State the preparation type.
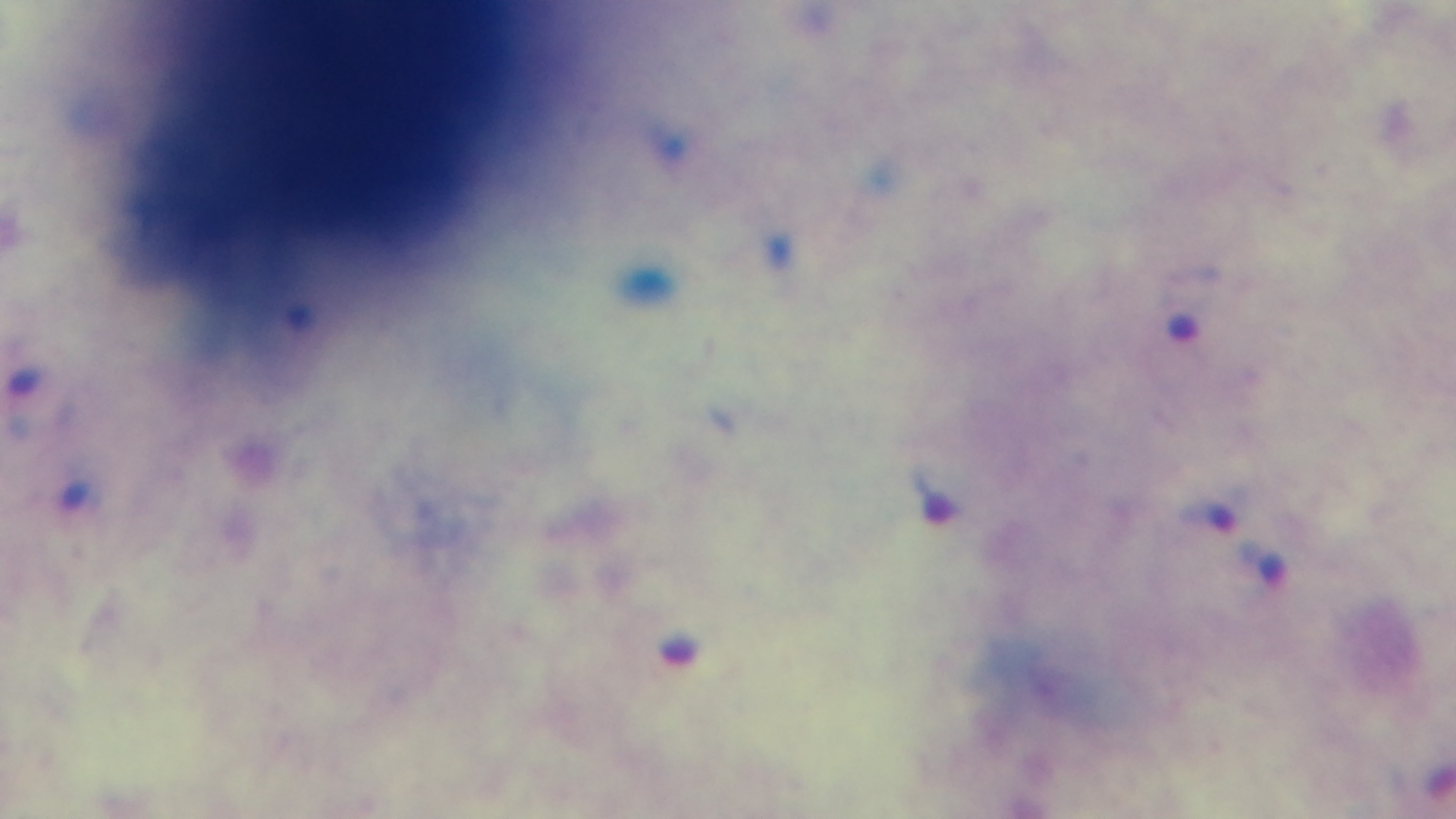

It is a thick blood film.

Malaria status: infected. 100x oil-immersion objective. Light microscopy. Giemsa stain. Captured with a mounted 4K digital camera. Single field of view.